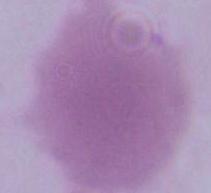
{
  "modality": "micrograph",
  "identification": "erythrocyte",
  "magnification": "1000x"
}